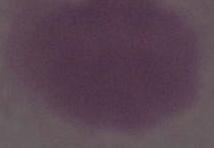
Summary:
  - Magnification: 1000x
  - Modality: micrograph
  - Identification: erythrocyte